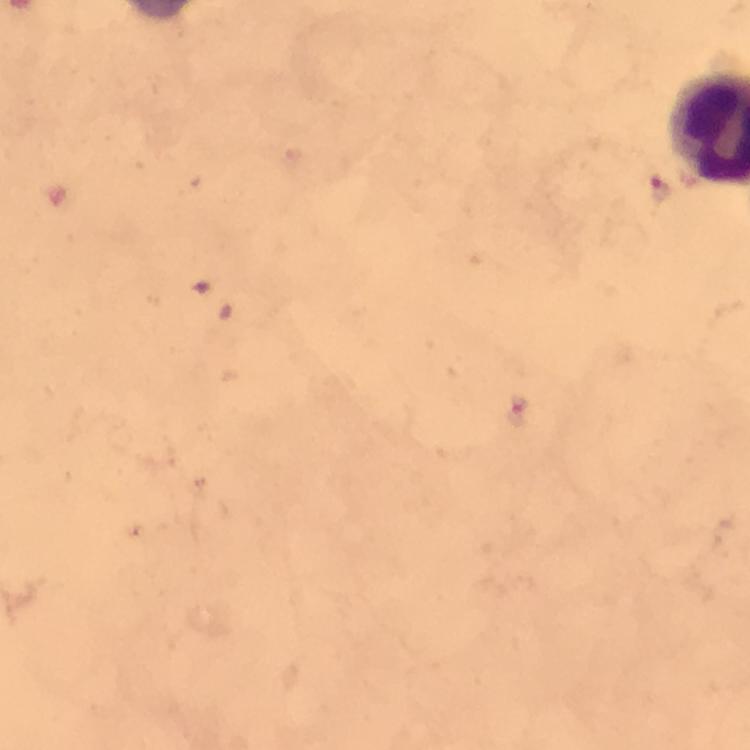
Approximate centers as {x, y} in pixels.
Summary:
  - Malaria parasite locations: {659, 190}, {516, 413}
  - Magnification: 100x
  - Capture: smartphone photograph through a microscope
  - Context: from a diagnostic examination for malaria
  - Immersion oil: used
  - Stain: Giemsa
  - Image size: 750×750 pixels
  - Preparation: thick blood film
  - Cropped from: one field of view